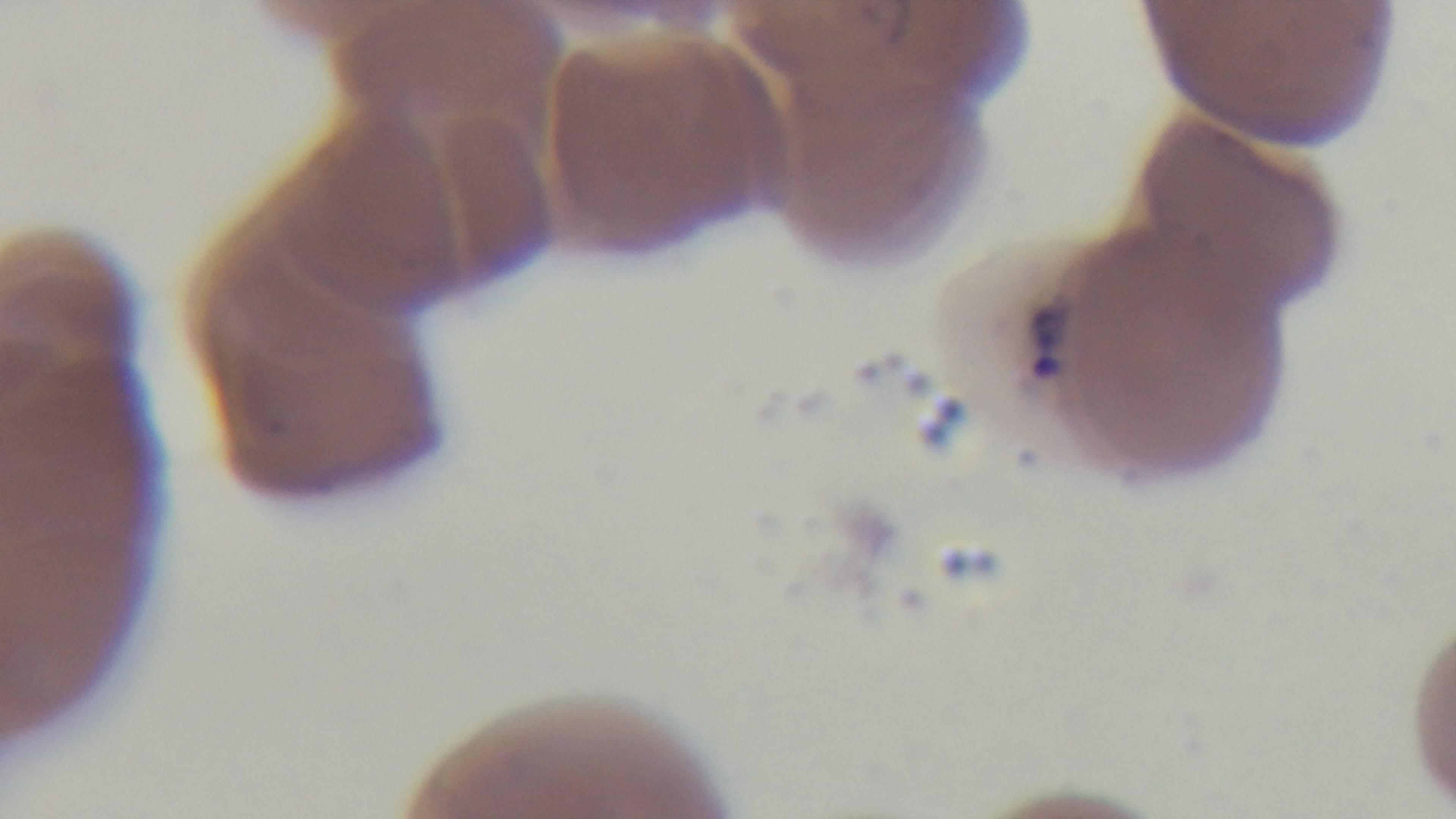
malaria status = positive
modality = light microscopy
preparation = thin blood film
capture = mounted 4K digital camera
objective = 100x oil immersion
field of view = one from the slide
stain = Giemsa